Outline each Plasmodium falciparum-infected red blood cell.
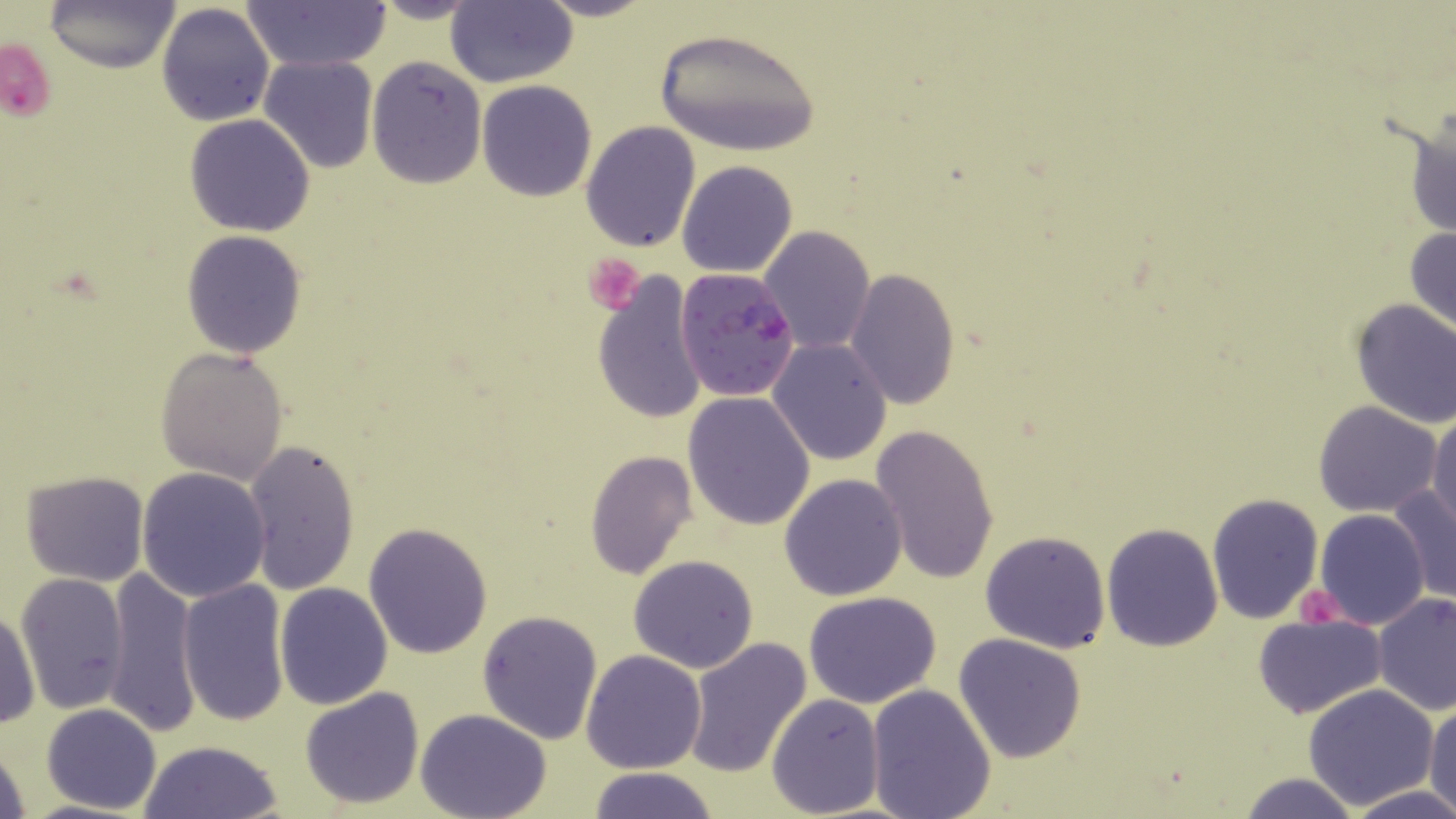

Approximate bounding boxes as (x1, y1, x2, y2) in pixels.
Plasmodium falciparum-infected red blood cells: (675, 266, 801, 402).

slide-level diagnosis = Plasmodium falciparum
image size = 1456×819 pixels
stain = May-Grünwald-Giemsa
platelet locations = approximate bounding boxes as (x1, y1, x2, y2) in pixels: (1, 37, 58, 127), (583, 252, 644, 314), (1296, 586, 1346, 629)
magnification = 1000x
modality = optical microscopy
preparation = thin blood film
field of view = one of a larger specimen
uninfected red blood cell locations = approximate bounding boxes as (x1, y1, x2, y2) in pixels: (45, 0, 179, 71), (365, 0, 486, 25), (534, 0, 661, 22), (445, 1, 577, 88), (245, 2, 388, 71), (156, 4, 275, 127), (653, 24, 821, 157), (260, 54, 378, 174), (366, 56, 487, 189), (478, 80, 598, 201), (1407, 105, 1455, 243), (185, 114, 316, 237), (580, 121, 701, 252), (677, 161, 797, 277), (759, 225, 874, 355), (1405, 225, 1456, 342), (181, 230, 307, 359), (846, 269, 960, 409), (591, 272, 708, 425), (1349, 298, 1456, 429), (767, 339, 893, 466), (155, 346, 289, 485), (683, 393, 816, 531), (1313, 401, 1443, 517), (1427, 409, 1456, 534), (869, 423, 1000, 587), (242, 438, 360, 595), (585, 451, 697, 579), (136, 468, 271, 602), (21, 469, 149, 586), (779, 473, 908, 601), (1388, 484, 1456, 604), (1206, 492, 1325, 625), (1314, 509, 1430, 629), (363, 521, 493, 658), (1100, 522, 1223, 652), (979, 530, 1112, 653), (629, 554, 760, 673), (106, 566, 201, 736), (15, 571, 131, 715), (177, 579, 289, 728), (275, 582, 393, 709), (804, 591, 945, 709), (1372, 593, 1456, 717), (1, 606, 40, 730), (477, 609, 603, 743), (1252, 612, 1388, 718), (952, 632, 1086, 762), (683, 636, 813, 779), (581, 650, 709, 774), (1303, 684, 1440, 808), (866, 685, 997, 818), (299, 687, 425, 809), (767, 691, 886, 816), (1426, 701, 1456, 814), (43, 703, 163, 814), (416, 710, 551, 819), (138, 739, 286, 819), (0, 740, 32, 819), (586, 768, 720, 819), (1236, 772, 1362, 819), (1344, 783, 1456, 819)